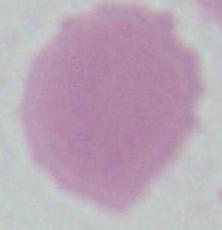

{
  "identification": "red blood cell",
  "modality": "micrograph",
  "magnification": "1000x"
}